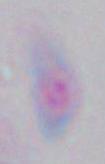
1000x magnification. Photomicrograph. Toxoplasma gondii is shown.